Assess this cell for malaria.
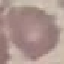

It is uninfected.

{
  "capture": "smartphone camera at the microscope eyepiece",
  "image_type": "cell patch, automatically extracted from a larger field of view and resized to 64 × 64 pixels",
  "preparation": "thin blood smear",
  "stain": "Giemsa"
}